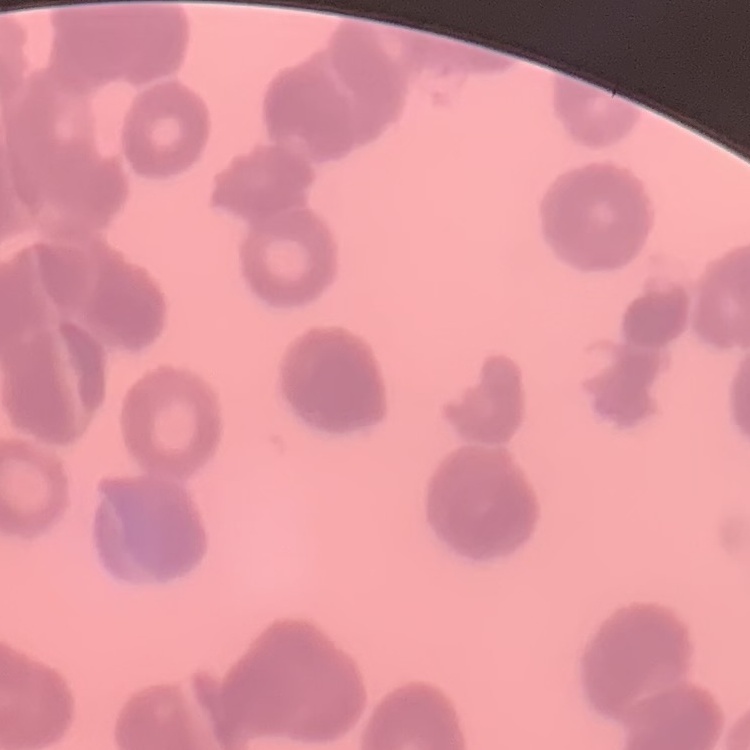
erythrocyte morphology = rouleaux formation
image type = one tile cut from a larger photomicrograph
preparation = thin peripheral smear
stain = Field's or Giemsa